Locate every malaria parasite.
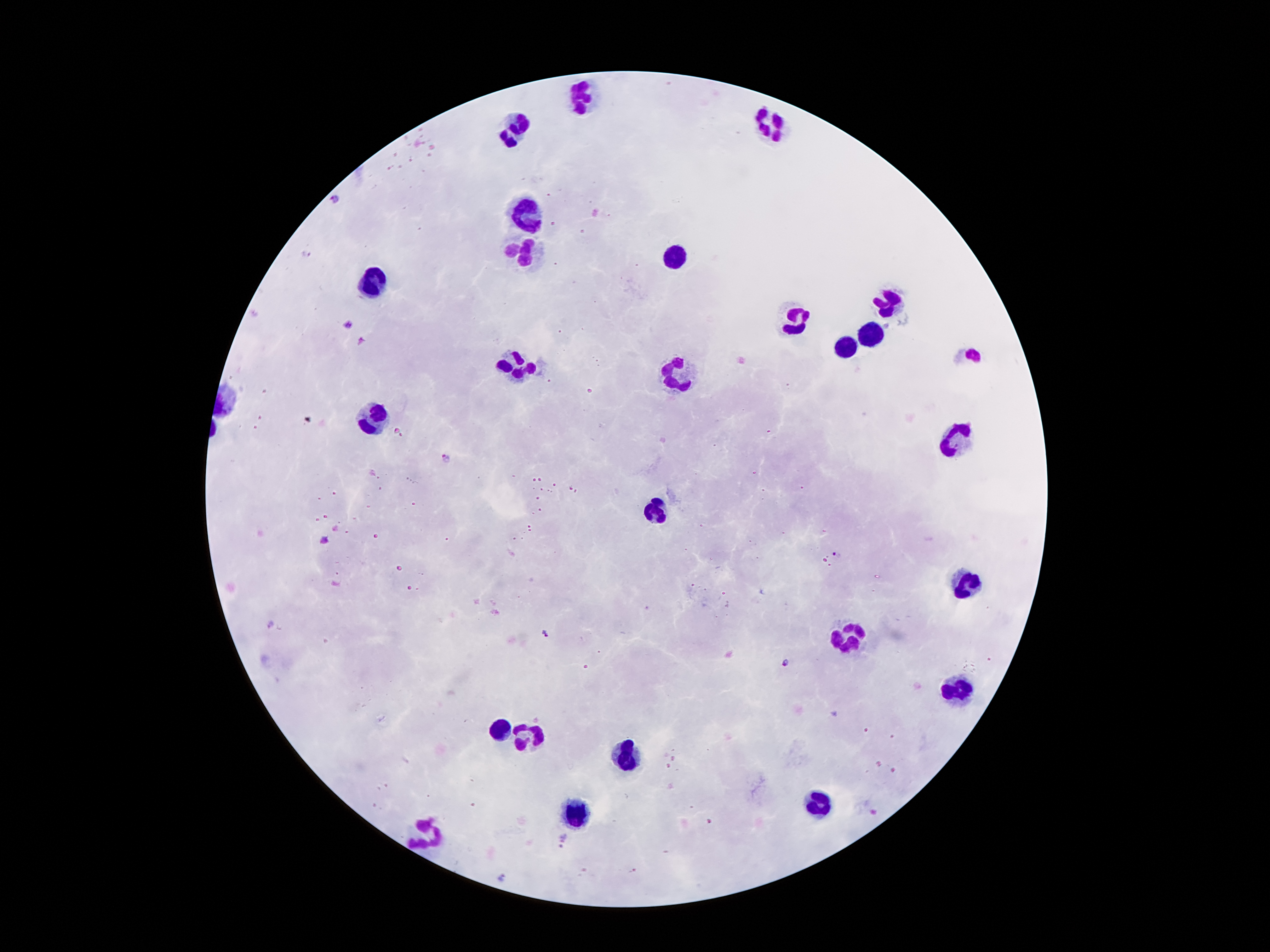

Approximate centers as {x, y} in pixels.
Malaria parasites: {335, 199}, {304, 254}, {349, 325}, {363, 342}, {445, 456}, {325, 539}, {838, 556}, {269, 624}, {545, 635}, {786, 663}, {564, 838}, {560, 846}, {502, 876}.

{
  "stain": "Giemsa",
  "capture": "smartphone through the microscope eyepiece",
  "leukocyte_locations": "approximate centers as {x, y} in pixels: {582, 96}, {777, 125}, {518, 132}, {526, 217}, {521, 252}, {673, 254}, {372, 283}, {890, 302}, {795, 320}, {872, 336}, {848, 348}, {974, 354}, {517, 364}, {677, 373}, {375, 416}, {954, 436}, {655, 511}, {965, 581}, {854, 635}, {956, 692}, {503, 724}, {533, 733}, {624, 754}, {818, 805}, {579, 814}, {429, 832}",
  "magnification": "100x",
  "patient_malaria_status": "infected with Plasmodium falciparum",
  "preparation": "thick peripheral-blood smear",
  "field_of_view": "single",
  "image_size": "1270×952 pixels"
}